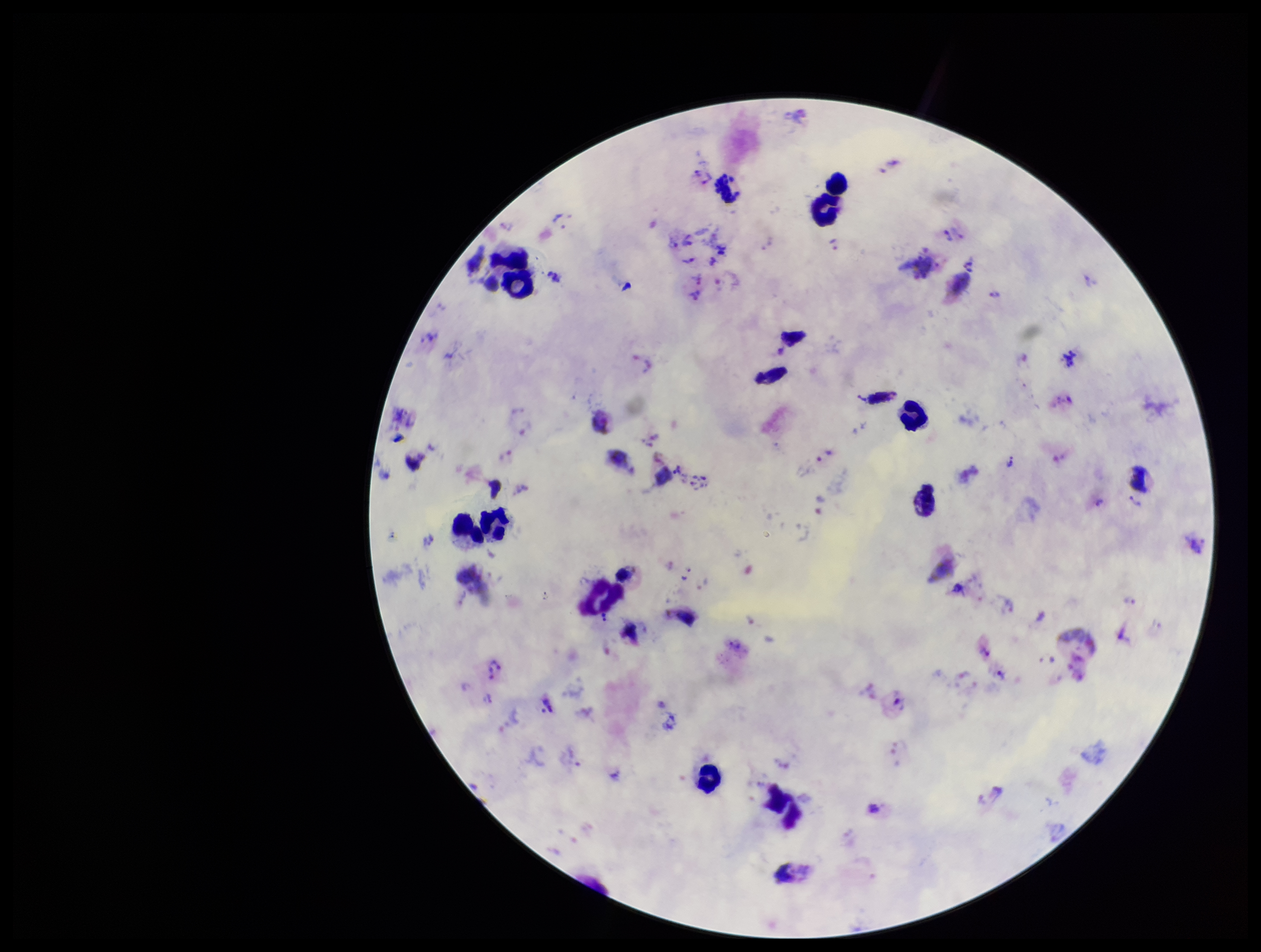
Summary:
  - Capture: smartphone photograph through the microscope eyepiece
  - Stain: Giemsa
  - Preparation: thick
  - Field of view: single
  - Plasmodium parasites: seen
  - Leukocyte count: 14
  - Image size: 1261×952 pixels
  - Patient malaria status: infected
  - Species reported for this patient: Plasmodium vivax
  - Parasite count: 47